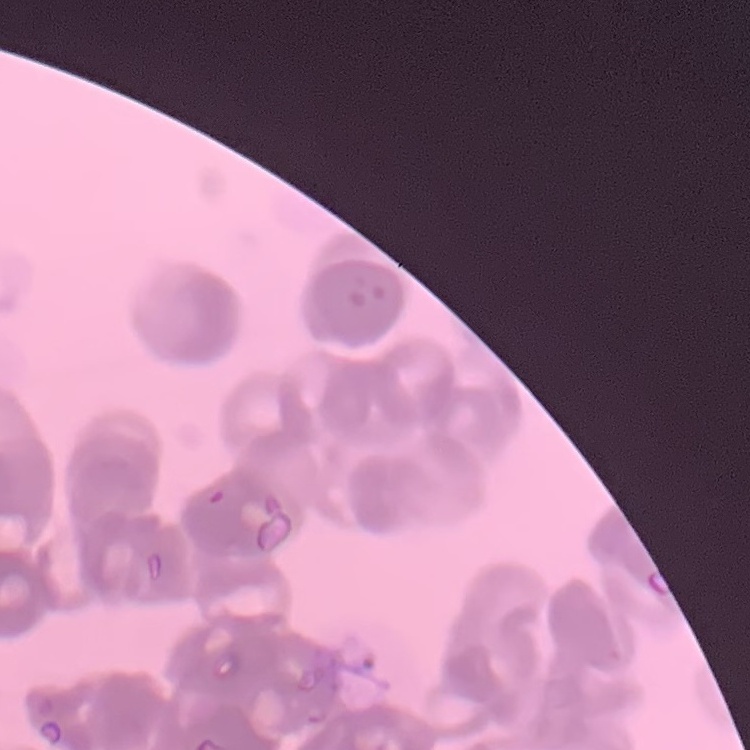

The red blood cells exhibit rouleaux formation. Stained with either Field's or Giemsa. Thin peripheral smear. One tile cut from a larger photomicrograph.